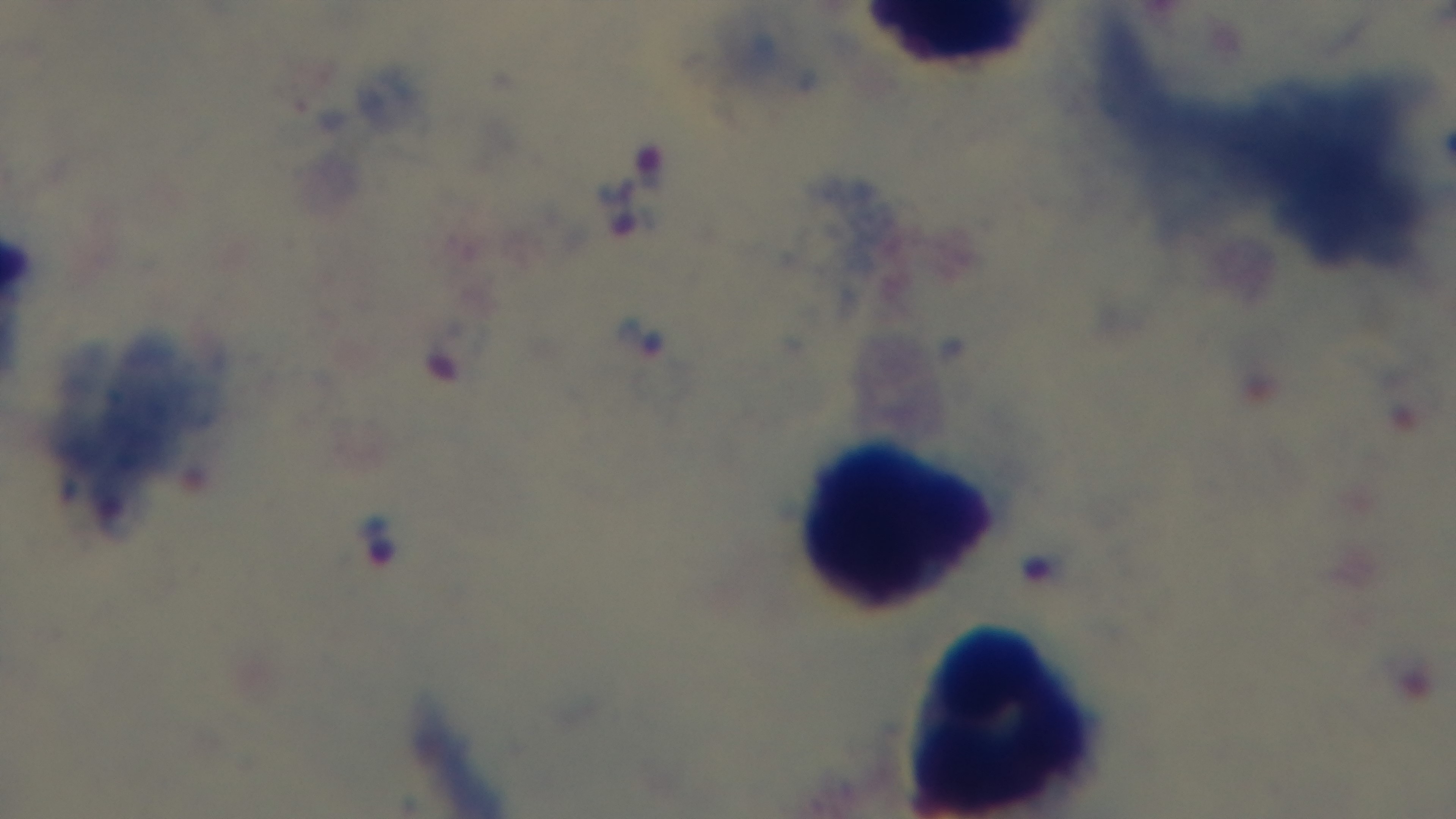

preparation: thick smear
objective: 100x oil immersion
capture: mounted 4K digital camera
malaria_status: positive
field_of_view: single
modality: light microscopy
stain: Giemsa